Assess this cell for malaria.
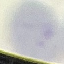
It is uninfected.

{
  "preparation": "thin blood film",
  "capture": "smartphone camera at the microscope eyepiece",
  "image_type": "cell patch, automatically extracted from a larger field of view and resized to 64 × 64 pixels",
  "stain": "Giemsa"
}